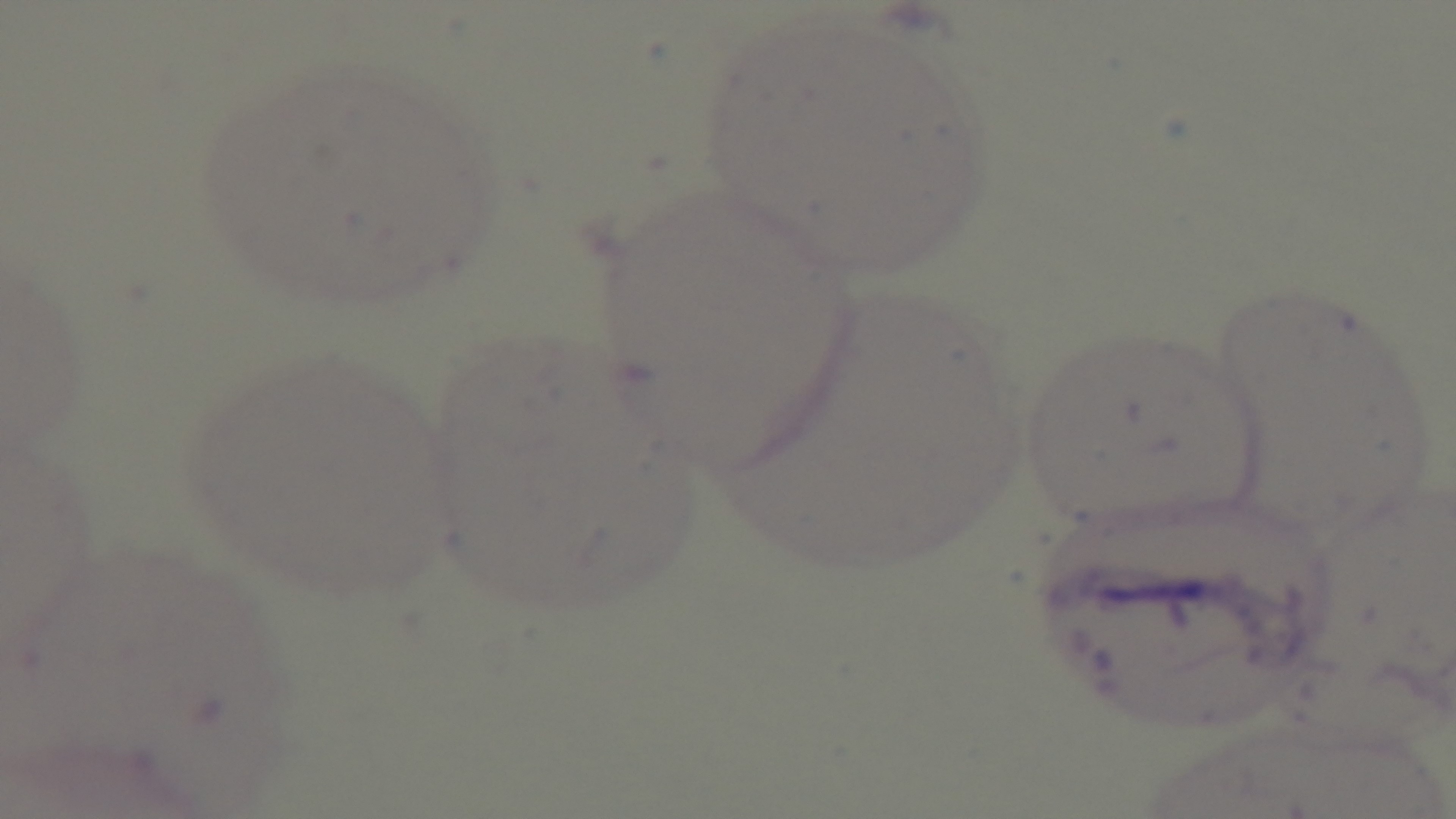

stain = Giemsa
field of view = single
objective = 100x oil immersion
capture = mounted 4K digital camera
modality = light microscopy
malaria status = negative
preparation = thin